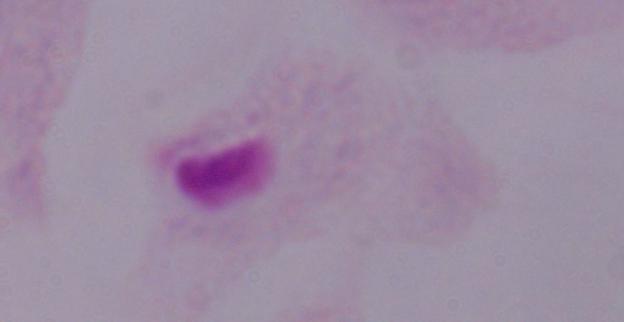

Photomicrograph. A trichomonad is shown. Captured at 1000x magnification.